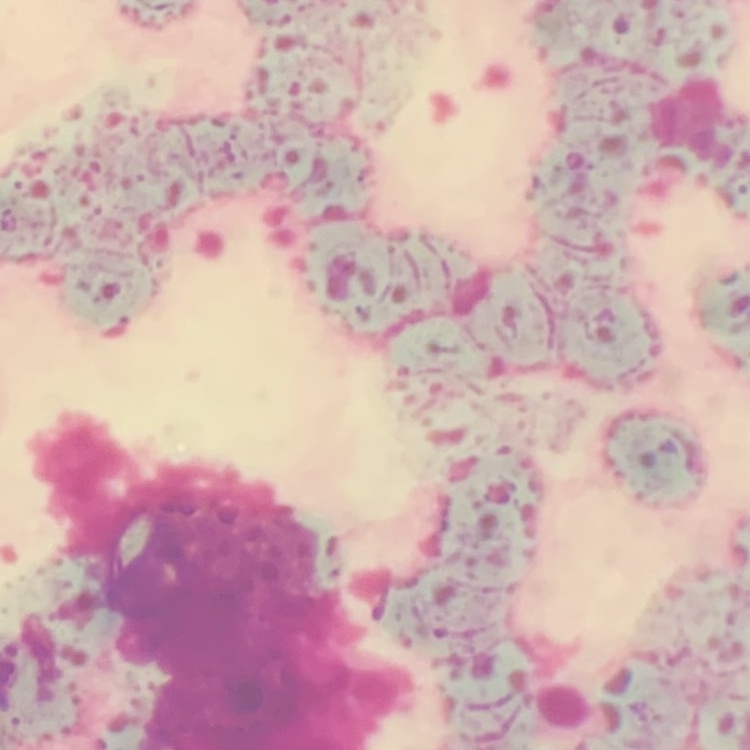
The red blood cells show rouleaux formation. Square crop of a larger photomicrograph. Thin peripheral smear. Field's or Giemsa stain.